Assess this cell for malaria.
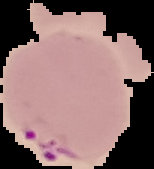
Parasitized.

Image is 154×169 pixels. From a thin blood smear. Segmented cell region on a black background.